Mark where platelets are.
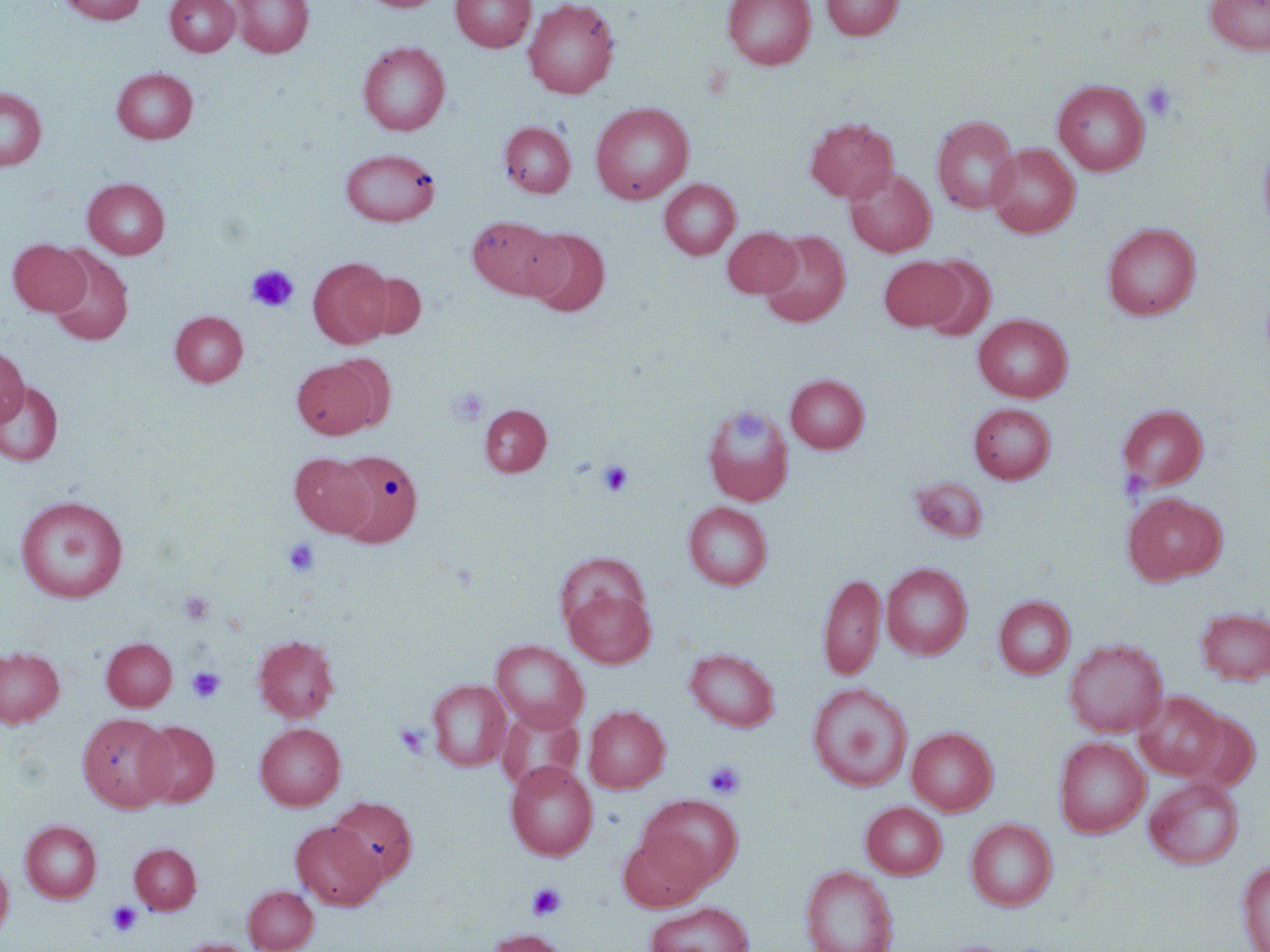
Approximate bounding boxes as (x1, y1, x2, y2) in pixels.
Platelets: (1141, 80, 1178, 121), (246, 264, 299, 313), (446, 387, 489, 426), (597, 459, 634, 497), (282, 537, 320, 576), (179, 590, 213, 626), (187, 666, 225, 703), (393, 722, 431, 757), (704, 759, 746, 799), (527, 882, 567, 921), (106, 900, 143, 936).

slide-level diagnosis = negative for blood parasites
magnification = 1000x
stain = May-Grünwald-Giemsa
field of view = single
modality = optical microscopy
image size = 1270×952 pixels
preparation = thin blood film
uninfected red blood cell locations = approximate bounding boxes as (x1, y1, x2, y2) in pixels: (59, 0, 146, 24), (165, 0, 239, 56), (230, 0, 314, 58), (361, 0, 444, 13), (451, 0, 535, 51), (523, 0, 619, 98), (723, 0, 815, 69), (821, 0, 902, 40), (1206, 0, 1269, 54), (358, 41, 450, 135), (112, 68, 197, 144), (1052, 79, 1150, 176), (0, 87, 47, 171), (590, 102, 694, 204), (932, 115, 1020, 214), (805, 117, 899, 203), (499, 121, 576, 198), (1257, 137, 1270, 243), (987, 143, 1080, 238), (340, 147, 440, 226), (845, 167, 936, 257), (83, 178, 170, 259), (659, 179, 740, 259), (467, 215, 562, 299), (1102, 223, 1201, 320), (723, 227, 801, 297), (523, 228, 610, 316), (759, 230, 850, 327), (9, 239, 91, 316), (47, 246, 134, 347), (919, 255, 996, 341), (879, 256, 963, 330), (309, 258, 391, 348), (357, 271, 426, 340), (170, 311, 249, 387), (973, 314, 1073, 401), (0, 347, 28, 427), (330, 354, 397, 430), (292, 359, 380, 439), (786, 375, 869, 453), (0, 382, 63, 466), (969, 402, 1056, 483), (480, 405, 551, 476), (703, 405, 794, 506), (1118, 405, 1208, 491), (333, 450, 423, 547), (291, 453, 375, 537), (910, 476, 988, 542), (1122, 493, 1227, 584), (15, 495, 128, 602), (683, 502, 772, 590), (882, 563, 972, 660), (819, 571, 886, 682), (564, 585, 656, 667), (994, 596, 1075, 679), (1195, 607, 1270, 685), (253, 636, 339, 722), (102, 637, 177, 710), (1063, 638, 1168, 737), (492, 640, 588, 731), (0, 647, 64, 727), (684, 648, 780, 732), (427, 679, 511, 771), (807, 683, 913, 792), (1134, 691, 1227, 780), (498, 704, 583, 792), (584, 705, 670, 793), (1179, 711, 1260, 792), (77, 713, 174, 812), (135, 720, 219, 807), (255, 722, 345, 810), (907, 727, 998, 815), (1055, 736, 1150, 838), (505, 761, 597, 861), (1144, 776, 1244, 869), (639, 793, 743, 888), (328, 797, 417, 885), (861, 801, 947, 879), (966, 819, 1057, 911), (20, 820, 101, 903), (291, 821, 385, 911), (618, 835, 707, 911), (130, 843, 201, 914), (0, 857, 13, 940), (1236, 860, 1270, 952), (800, 865, 899, 952), (244, 885, 319, 952), (644, 901, 755, 952), (486, 929, 569, 952), (177, 939, 257, 952)